Classify this cell by malaria status.
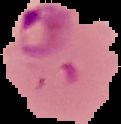

It is parasitized.

Image is 121×124 pixels. The area outside the segmented cell region is set to black. From a thin blood film.